Mark where platelets are.
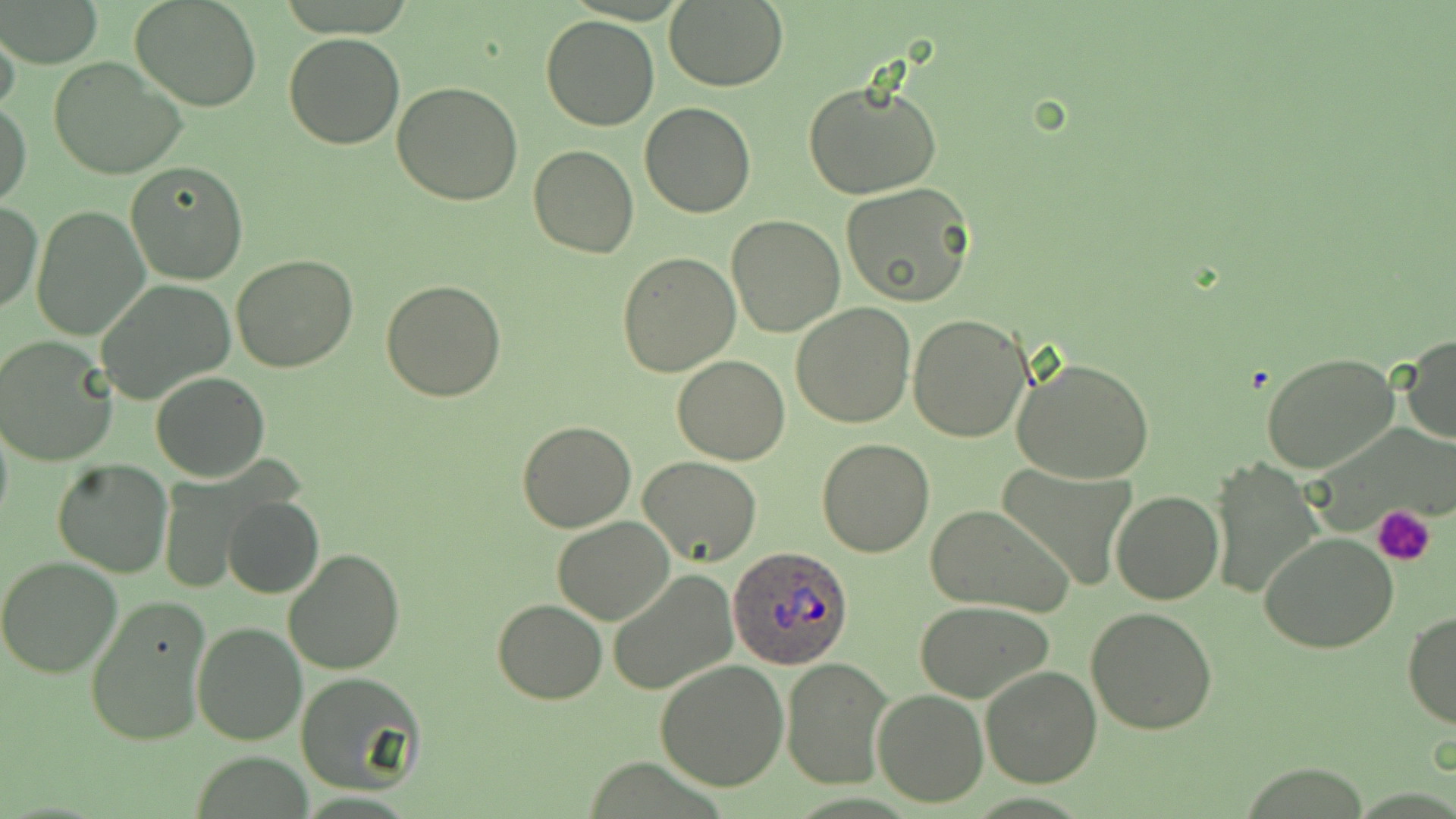
Approximate bounding boxes as [x1, y1, x2, y2] in pixels.
Platelets: [1375, 506, 1437, 566].

slide-level diagnosis = Plasmodium ovale
uninfected red blood cell locations = approximate bounding boxes as [x1, y1, x2, y2] in pixels: [1, 0, 100, 67], [131, 0, 261, 112], [664, 2, 788, 91], [542, 14, 658, 131], [0, 22, 22, 120], [283, 33, 406, 149], [47, 56, 187, 180], [803, 79, 942, 200], [393, 81, 524, 204], [0, 97, 31, 210], [640, 103, 755, 218], [530, 144, 639, 258], [126, 162, 248, 284], [840, 183, 975, 307], [1, 200, 43, 315], [30, 205, 151, 340], [726, 215, 847, 337], [617, 251, 740, 376], [231, 254, 358, 373], [94, 280, 236, 405], [381, 280, 507, 403], [790, 303, 915, 428], [907, 314, 1033, 444], [1401, 333, 1456, 447], [1, 335, 120, 467], [1260, 352, 1400, 475], [672, 354, 789, 465], [1012, 356, 1155, 484], [151, 372, 270, 482], [0, 408, 13, 540], [516, 419, 636, 533], [816, 437, 935, 557], [638, 454, 761, 565], [51, 458, 174, 578], [1208, 460, 1324, 600], [995, 466, 1138, 591], [1112, 491, 1224, 605], [223, 496, 325, 599], [923, 505, 1072, 617], [552, 515, 674, 624], [1259, 532, 1399, 654], [284, 548, 405, 675], [0, 556, 123, 678], [607, 568, 740, 698], [83, 596, 213, 748], [493, 600, 606, 703], [915, 600, 1055, 703], [1086, 606, 1218, 735], [1402, 610, 1456, 730], [191, 621, 306, 745], [780, 656, 894, 790], [654, 660, 789, 791], [980, 665, 1103, 787], [298, 673, 426, 796], [871, 689, 990, 807]
stain = May-Grünwald-Giemsa
Plasmodium ovale-infected red blood cell locations = approximate bounding boxes as [x1, y1, x2, y2] in pixels: [728, 547, 853, 668]
magnification = 1000x
field of view = single
preparation = thin blood film
modality = light microscopy
image size = 1456×819 pixels